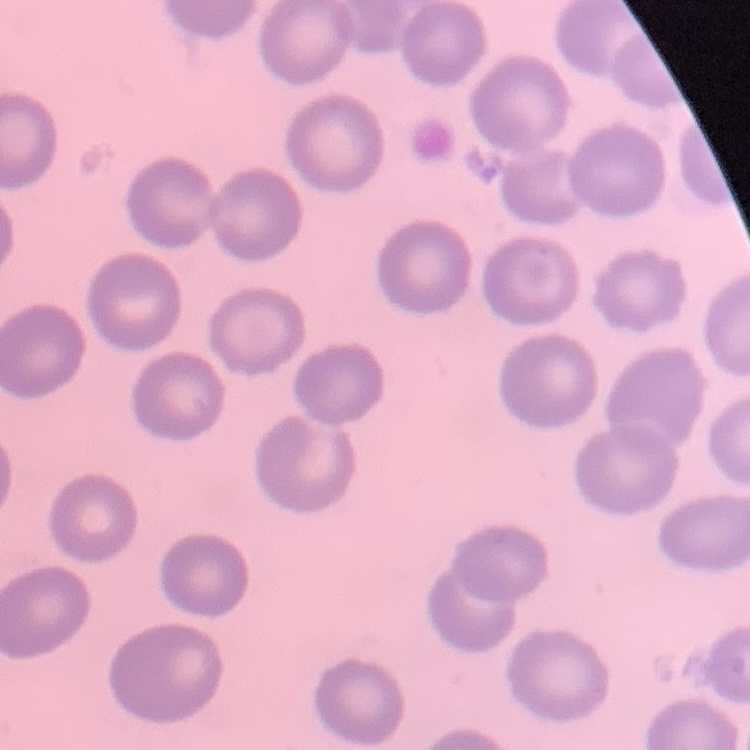

The red blood cells show no rouleaux formation. One tile cut from a larger photomicrograph. Stained with either Field's or Giemsa. Thin blood smear.